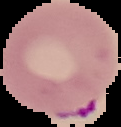

Summary:
  - Image type: cell region segmented out of the field of view; surrounding area masked to black
  - Image size: 121×127 pixels
  - Preparation: thin blood film
  - Result: malaria parasites detected